Identify the preparation type.
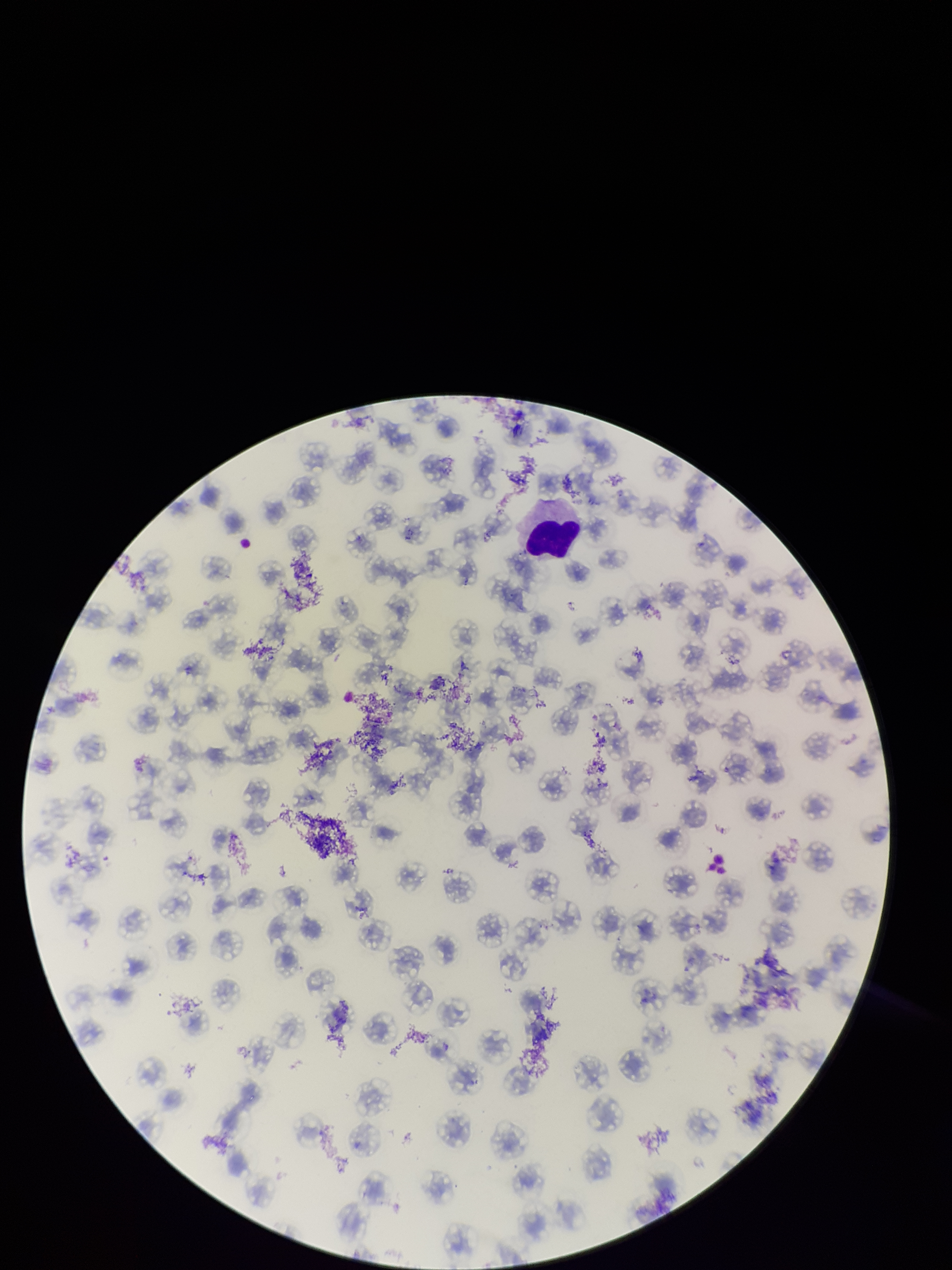

A thin smear.

Red blood cell count: 105. One field from this slide. Photographed through the microscope eyepiece with a smartphone camera. Stained with Giemsa. Image is 952×1270 pixels. Parasitized red blood cells: none detected. Patient malaria status: infected. Parasitized red blood cell count: 0. Species reported for this patient: Plasmodium falciparum.